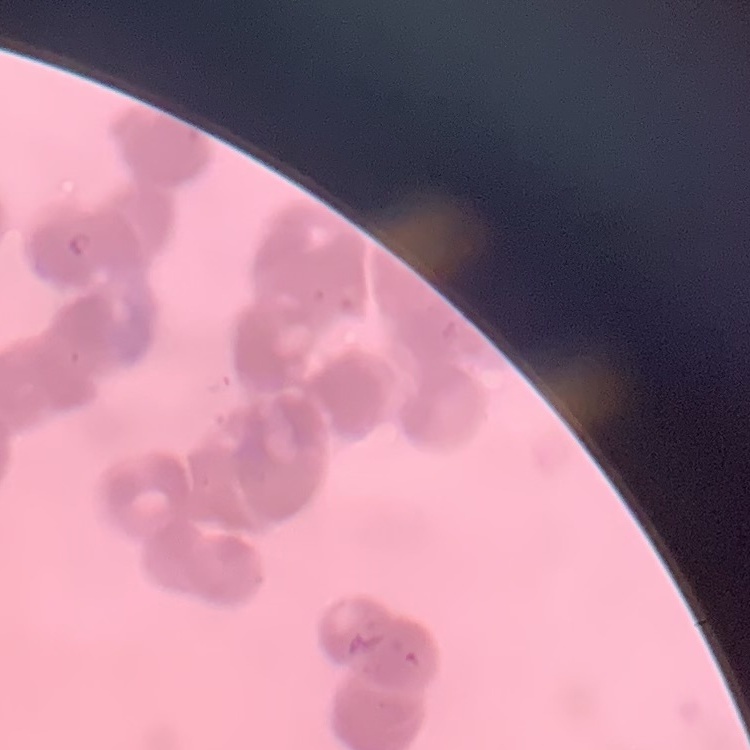
Summary:
  - Erythrocyte morphology: rouleaux formation
  - Image type: square crop of a larger photomicrograph
  - Stain: Field's or Giemsa
  - Preparation: thin blood smear